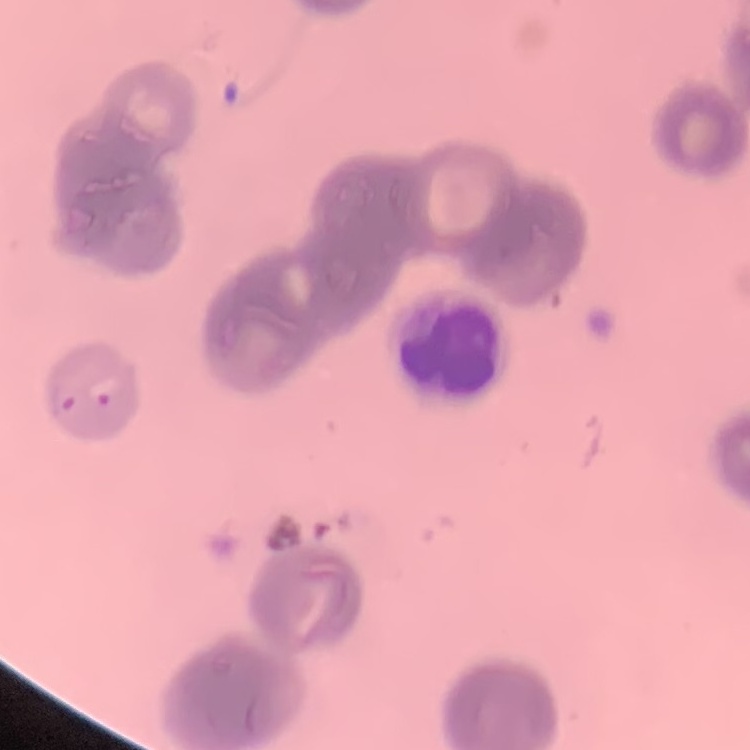

red_blood_cell_morphology: rouleaux formation
preparation: thin blood smear
stain: Field's or Giemsa
image_type: square crop of a larger photomicrograph